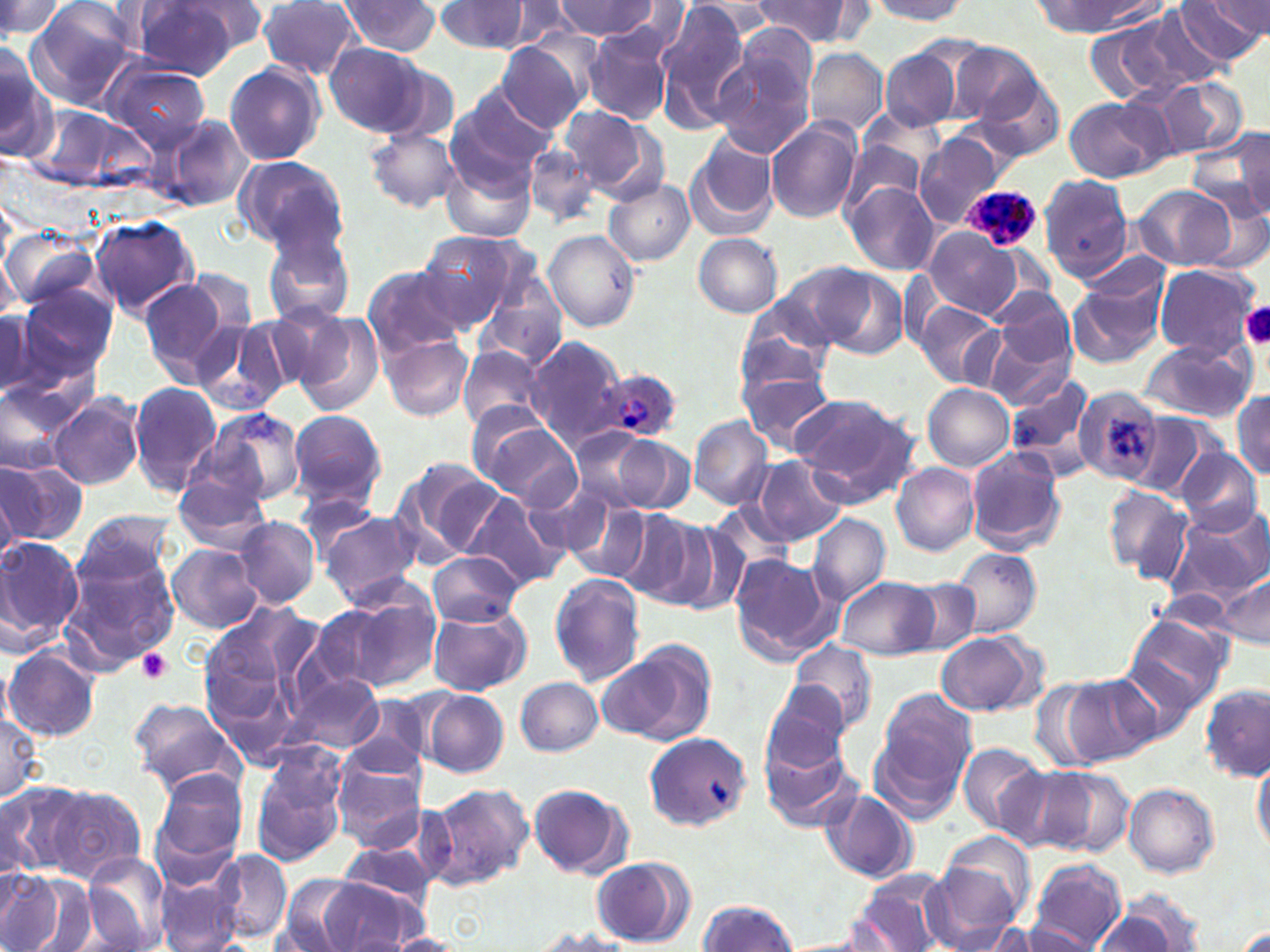

Approximate bounding boxes as (x1,y1)-(x2,y2) corner pairs in pixels. Platelet locations: (1240,302)-(1270,349), (137,649)-(174,683). Uninfected red blood cell locations: (0,0)-(62,43), (554,0)-(658,39), (866,0)-(970,22), (1178,0)-(1268,61), (181,1)-(272,52), (654,1)-(754,125), (1038,1)-(1158,35), (25,2)-(140,108), (126,2)-(246,77), (258,2)-(362,80), (335,2)-(442,55), (434,2)-(533,53), (483,2)-(584,52), (694,2)-(780,38), (753,2)-(851,44), (1150,2)-(1253,86), (607,4)-(693,63), (1098,7)-(1214,102), (734,23)-(824,104), (582,29)-(672,124), (497,41)-(589,133), (948,41)-(1042,127), (325,42)-(430,137), (806,49)-(886,137), (882,49)-(962,132), (712,51)-(815,156), (0,54)-(57,164), (103,61)-(211,152), (224,63)-(326,166), (973,75)-(1067,163), (1154,77)-(1248,160), (449,88)-(557,184), (1065,98)-(1167,182), (28,103)-(149,193), (561,105)-(651,195), (163,114)-(252,212), (765,118)-(861,224), (364,127)-(462,213), (1217,127)-(1270,218), (687,134)-(779,237), (915,134)-(1002,227), (840,139)-(926,217), (522,143)-(601,225), (232,155)-(348,255), (441,155)-(535,244), (1039,174)-(1134,281), (604,179)-(695,266), (844,182)-(941,274), (1131,185)-(1238,271), (1196,198)-(1269,276), (90,215)-(200,319), (1,227)-(100,313), (925,228)-(1023,319), (543,229)-(642,332), (416,230)-(522,329), (264,231)-(356,329), (693,234)-(783,318), (773,261)-(880,352), (362,263)-(470,358), (1151,263)-(1260,357), (817,268)-(909,362), (138,274)-(239,383), (1066,274)-(1166,369), (475,283)-(567,368), (17,284)-(118,383), (916,302)-(1003,388), (257,307)-(354,393), (1,309)-(39,398), (287,309)-(385,413), (735,314)-(833,404), (976,315)-(1077,408), (190,318)-(295,418), (381,333)-(473,420), (528,334)-(630,448), (1138,340)-(1255,423), (458,345)-(550,434), (8,350)-(99,440), (739,367)-(835,456), (1005,373)-(1100,483), (0,381)-(77,476), (128,381)-(222,495), (1073,383)-(1165,488), (923,384)-(1014,471), (1232,390)-(1270,478), (49,393)-(146,491), (789,393)-(918,501), (200,406)-(308,509), (288,408)-(387,512), (1124,413)-(1213,501), (473,414)-(581,510), (690,416)-(774,510), (569,425)-(660,514), (602,433)-(696,515), (964,446)-(1066,555), (1177,449)-(1263,533), (753,456)-(848,547), (391,459)-(503,563), (0,460)-(86,546), (891,464)-(979,556), (0,465)-(42,552), (172,472)-(272,551), (527,479)-(638,567), (1102,484)-(1192,584), (458,491)-(571,591), (295,494)-(381,563), (561,496)-(655,583), (709,502)-(794,574), (1162,507)-(1270,610), (74,508)-(180,593), (317,509)-(424,605), (613,509)-(711,606), (807,514)-(890,604), (232,516)-(320,608), (667,525)-(753,617), (0,535)-(83,647), (167,544)-(263,633), (951,546)-(1041,638), (429,549)-(522,628), (58,553)-(181,672), (728,553)-(840,665), (1213,570)-(1269,652), (548,573)-(644,684), (837,575)-(941,660), (905,580)-(979,653), (309,593)-(435,695), (198,598)-(321,762), (427,606)-(531,696), (1122,611)-(1234,712), (935,632)-(1042,716), (788,639)-(878,736), (601,641)-(715,746), (3,646)-(99,742), (284,672)-(384,755), (1049,675)-(1158,768), (516,677)-(603,756), (761,682)-(853,771), (1201,685)-(1268,781), (878,688)-(978,792), (421,690)-(509,778), (344,696)-(430,779), (128,697)-(243,792), (0,704)-(44,803), (645,731)-(750,833), (759,732)-(860,833), (870,732)-(963,824), (958,743)-(1047,834), (245,747)-(349,865), (331,757)-(426,852), (1252,759)-(1270,854), (995,762)-(1097,851), (1038,766)-(1135,858), (149,767)-(250,876), (526,781)-(632,878), (0,782)-(79,881), (425,782)-(534,888), (1123,783)-(1219,877), (44,787)-(147,884), (820,791)-(917,884), (942,830)-(1036,918), (335,844)-(442,910), (213,849)-(292,943), (923,853)-(1029,950), (77,854)-(174,952), (588,855)-(695,946), (1026,859)-(1127,951), (0,869)-(67,952), (850,871)-(952,952), (275,872)-(371,951), (19,875)-(102,952), (157,877)-(243,952), (316,877)-(426,951), (1109,891)-(1209,950), (696,899)-(799,951), (1090,909)-(1180,952), (1229,921)-(1269,952), (523,925)-(641,952), (1016,925)-(1099,950), (382,933)-(469,952). Plasmodium ovale-infected red blood cell locations: (964,185)-(1040,251), (598,368)-(683,442). Slide-level diagnosis: Plasmodium ovale. Image is 1270×952 pixels. Optical microscopy. Captured at 1000x magnification. Single field of view. Thin blood smear. May-Grünwald-Giemsa stain.